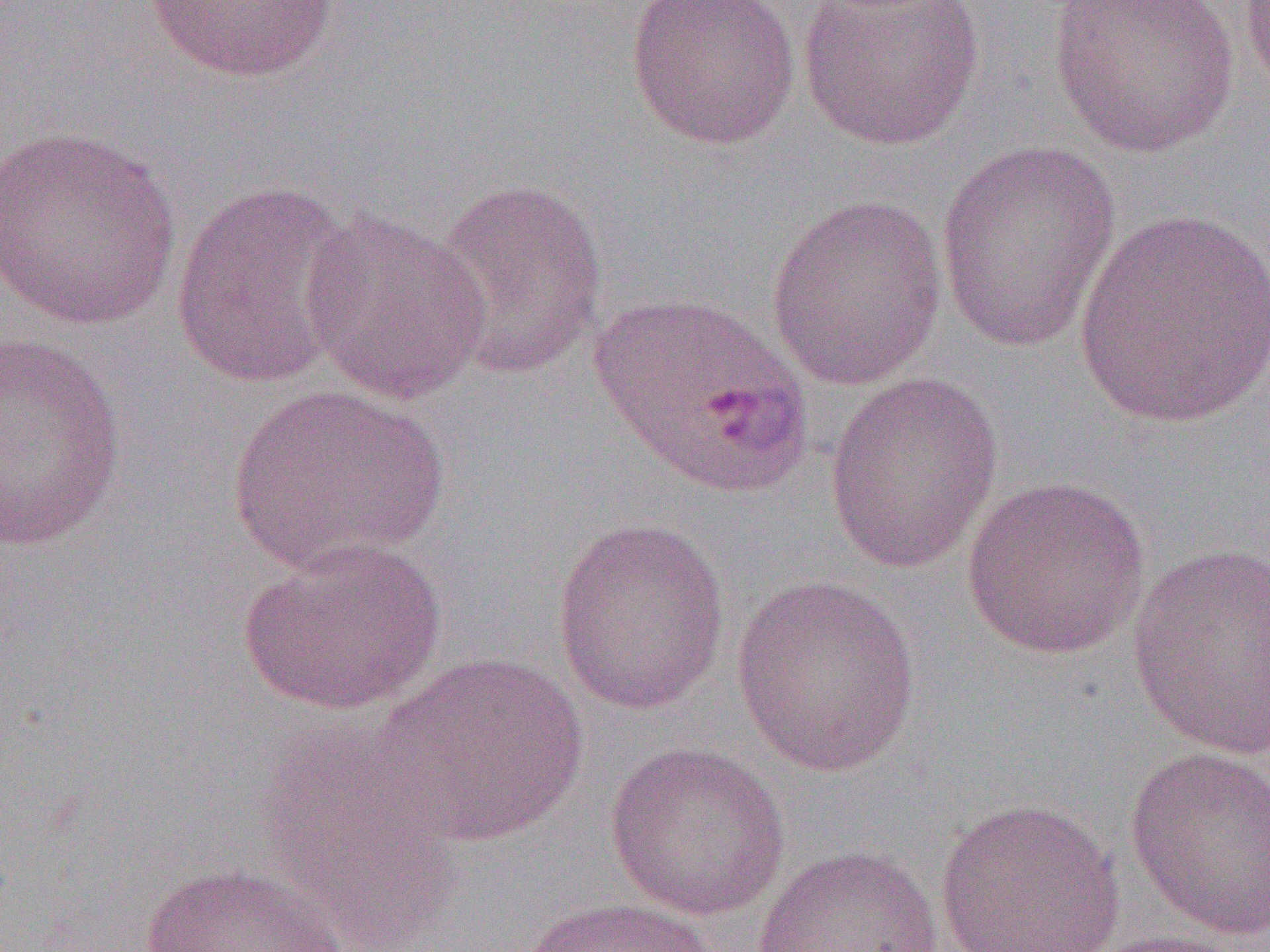
{
  "slide_level_diagnosis": "Plasmodium ovale",
  "modality": "optical microscopy",
  "preparation": "thin blood film",
  "image_size": "1270×952 pixels",
  "field_of_view": "one of a larger specimen",
  "uninfected_red_blood_cell_locations": "approximate bounding boxes as named x1/y1/x2/y2 corners in pixels: (x1=625, y1=0, x2=801, y2=151), (x1=799, y1=0, x2=986, y2=152), (x1=1048, y1=0, x2=1240, y2=159), (x1=1239, y1=0, x2=1270, y2=103), (x1=144, y1=1, x2=340, y2=83), (x1=0, y1=125, x2=183, y2=330), (x1=935, y1=141, x2=1122, y2=354), (x1=431, y1=178, x2=610, y2=380), (x1=169, y1=180, x2=363, y2=391), (x1=765, y1=193, x2=948, y2=391), (x1=1075, y1=207, x2=1269, y2=431), (x1=301, y1=210, x2=492, y2=406), (x1=589, y1=289, x2=814, y2=500), (x1=1, y1=330, x2=128, y2=555), (x1=823, y1=371, x2=1003, y2=573), (x1=226, y1=383, x2=449, y2=574), (x1=961, y1=475, x2=1150, y2=660), (x1=550, y1=516, x2=731, y2=715), (x1=236, y1=537, x2=447, y2=716), (x1=1126, y1=541, x2=1270, y2=761), (x1=730, y1=574, x2=923, y2=777), (x1=373, y1=652, x2=589, y2=847), (x1=255, y1=733, x2=464, y2=947), (x1=604, y1=741, x2=791, y2=922), (x1=1124, y1=744, x2=1270, y2=942), (x1=935, y1=798, x2=1125, y2=952), (x1=751, y1=845, x2=944, y2=952), (x1=138, y1=860, x2=350, y2=952), (x1=519, y1=896, x2=720, y2=952), (x1=1083, y1=928, x2=1255, y2=952)",
  "magnification": "1000x"
}